Report the malaria status of this cell.
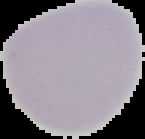

Uninfected.

From a thin blood film. Image is 145×139 pixels. Segmented cell region on a black background.